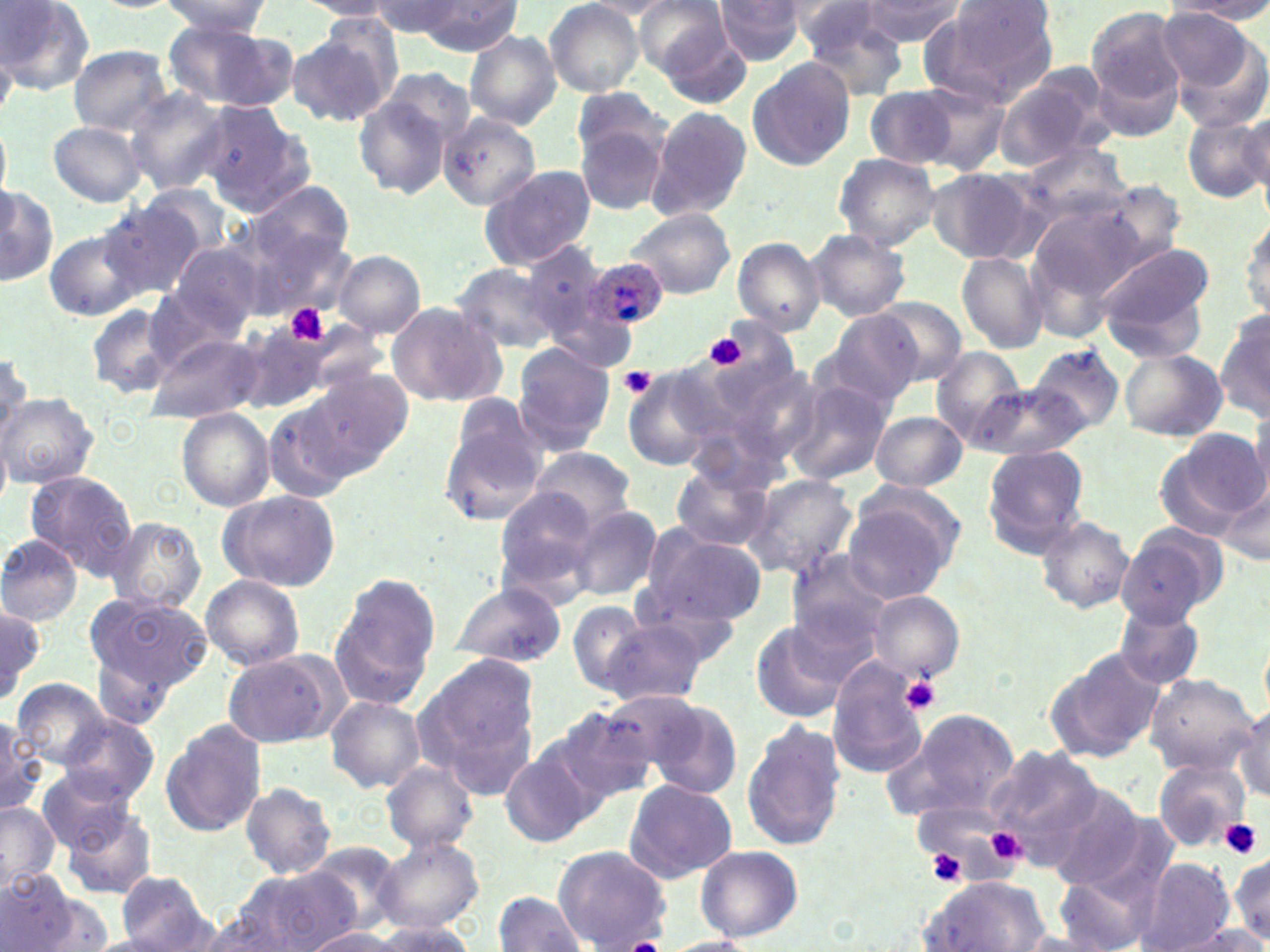
Approximate bounding boxes as named x1/y1/x2/y2 corners in pixels. Platelet locations: (x1=285, y1=303, x2=327, y2=345), (x1=695, y1=326, x2=761, y2=381), (x1=705, y1=336, x2=746, y2=369), (x1=620, y1=366, x2=657, y2=401), (x1=899, y1=676, x2=942, y2=714), (x1=1220, y1=818, x2=1263, y2=859), (x1=983, y1=825, x2=1026, y2=867), (x1=928, y1=849, x2=968, y2=885). Plasmodium ovale-infected red blood cell locations: (x1=583, y1=257, x2=670, y2=334). Uninfected red blood cell locations: (x1=0, y1=0, x2=95, y2=91), (x1=158, y1=0, x2=270, y2=39), (x1=371, y1=0, x2=463, y2=37), (x1=632, y1=0, x2=739, y2=83), (x1=859, y1=0, x2=963, y2=46), (x1=937, y1=0, x2=1060, y2=94), (x1=299, y1=1, x2=400, y2=20), (x1=544, y1=1, x2=645, y2=97), (x1=577, y1=1, x2=681, y2=17), (x1=713, y1=1, x2=806, y2=65), (x1=1166, y1=1, x2=1270, y2=20), (x1=414, y1=2, x2=522, y2=54), (x1=797, y1=3, x2=913, y2=98), (x1=158, y1=4, x2=280, y2=82), (x1=1160, y1=9, x2=1265, y2=108), (x1=1086, y1=10, x2=1187, y2=137), (x1=172, y1=24, x2=296, y2=111), (x1=286, y1=25, x2=397, y2=128), (x1=653, y1=27, x2=753, y2=108), (x1=465, y1=30, x2=562, y2=129), (x1=69, y1=46, x2=171, y2=135), (x1=746, y1=57, x2=857, y2=172), (x1=995, y1=70, x2=1109, y2=170), (x1=913, y1=83, x2=1012, y2=175), (x1=352, y1=87, x2=462, y2=200), (x1=571, y1=87, x2=669, y2=171), (x1=122, y1=88, x2=233, y2=196), (x1=865, y1=88, x2=961, y2=169), (x1=191, y1=102, x2=317, y2=215), (x1=643, y1=106, x2=753, y2=222), (x1=1241, y1=108, x2=1270, y2=195), (x1=440, y1=111, x2=541, y2=210), (x1=573, y1=114, x2=672, y2=219), (x1=1184, y1=115, x2=1269, y2=202), (x1=47, y1=121, x2=148, y2=207), (x1=1022, y1=141, x2=1132, y2=224), (x1=833, y1=153, x2=941, y2=248), (x1=478, y1=164, x2=597, y2=271), (x1=927, y1=166, x2=1047, y2=265), (x1=250, y1=181, x2=354, y2=268), (x1=1098, y1=181, x2=1189, y2=266), (x1=0, y1=183, x2=56, y2=289), (x1=139, y1=183, x2=235, y2=256), (x1=98, y1=202, x2=202, y2=299), (x1=1027, y1=204, x2=1148, y2=312), (x1=623, y1=207, x2=736, y2=298), (x1=1240, y1=212, x2=1270, y2=323), (x1=235, y1=220, x2=354, y2=321), (x1=46, y1=227, x2=147, y2=322), (x1=806, y1=228, x2=910, y2=321), (x1=733, y1=238, x2=826, y2=336), (x1=166, y1=240, x2=263, y2=336), (x1=521, y1=240, x2=613, y2=350), (x1=1098, y1=243, x2=1213, y2=355), (x1=333, y1=251, x2=425, y2=338), (x1=956, y1=252, x2=1048, y2=354), (x1=452, y1=262, x2=563, y2=357), (x1=867, y1=296, x2=968, y2=385), (x1=384, y1=299, x2=507, y2=407), (x1=86, y1=302, x2=182, y2=400), (x1=1216, y1=306, x2=1269, y2=424), (x1=817, y1=311, x2=924, y2=407), (x1=233, y1=327, x2=353, y2=413), (x1=147, y1=332, x2=262, y2=422), (x1=1025, y1=343, x2=1124, y2=438), (x1=512, y1=344, x2=615, y2=455), (x1=0, y1=347, x2=32, y2=446), (x1=1118, y1=347, x2=1227, y2=441), (x1=932, y1=348, x2=1025, y2=449), (x1=311, y1=368, x2=413, y2=468), (x1=623, y1=374, x2=720, y2=470), (x1=785, y1=379, x2=893, y2=485), (x1=974, y1=380, x2=1090, y2=463), (x1=2, y1=394, x2=99, y2=488), (x1=265, y1=401, x2=356, y2=500), (x1=179, y1=410, x2=276, y2=511), (x1=439, y1=410, x2=546, y2=525), (x1=870, y1=410, x2=969, y2=491), (x1=1156, y1=428, x2=1266, y2=539), (x1=982, y1=446, x2=1088, y2=555), (x1=526, y1=447, x2=638, y2=535), (x1=669, y1=463, x2=774, y2=551), (x1=25, y1=471, x2=138, y2=578), (x1=743, y1=474, x2=858, y2=580), (x1=1216, y1=478, x2=1269, y2=571), (x1=494, y1=486, x2=602, y2=595), (x1=218, y1=490, x2=340, y2=591), (x1=842, y1=500, x2=954, y2=603), (x1=568, y1=505, x2=662, y2=601), (x1=1035, y1=515, x2=1134, y2=613), (x1=105, y1=517, x2=207, y2=616), (x1=1116, y1=525, x2=1226, y2=628), (x1=641, y1=529, x2=767, y2=628), (x1=0, y1=535, x2=84, y2=627), (x1=785, y1=550, x2=895, y2=648), (x1=328, y1=571, x2=441, y2=709), (x1=202, y1=574, x2=304, y2=671), (x1=450, y1=584, x2=568, y2=667), (x1=631, y1=584, x2=743, y2=668), (x1=866, y1=591, x2=964, y2=681), (x1=86, y1=595, x2=213, y2=693), (x1=567, y1=599, x2=650, y2=693), (x1=783, y1=601, x2=886, y2=692), (x1=0, y1=603, x2=43, y2=703), (x1=1115, y1=605, x2=1205, y2=691), (x1=597, y1=619, x2=706, y2=707), (x1=749, y1=619, x2=855, y2=724), (x1=91, y1=647, x2=176, y2=730), (x1=1046, y1=647, x2=1166, y2=761), (x1=224, y1=650, x2=343, y2=750), (x1=413, y1=651, x2=541, y2=797), (x1=827, y1=665, x2=931, y2=778), (x1=1142, y1=673, x2=1257, y2=777), (x1=10, y1=676, x2=109, y2=767), (x1=618, y1=689, x2=743, y2=798), (x1=326, y1=695, x2=425, y2=793), (x1=1235, y1=701, x2=1270, y2=801), (x1=541, y1=705, x2=657, y2=812), (x1=881, y1=708, x2=1022, y2=826), (x1=56, y1=713, x2=159, y2=806), (x1=0, y1=717, x2=43, y2=816), (x1=740, y1=719, x2=848, y2=853), (x1=160, y1=720, x2=266, y2=838), (x1=498, y1=746, x2=598, y2=849), (x1=988, y1=747, x2=1105, y2=863), (x1=1152, y1=757, x2=1249, y2=852), (x1=381, y1=760, x2=477, y2=853), (x1=35, y1=769, x2=137, y2=856), (x1=623, y1=779, x2=737, y2=883), (x1=238, y1=783, x2=338, y2=879), (x1=1040, y1=784, x2=1152, y2=891), (x1=0, y1=801, x2=61, y2=891), (x1=61, y1=809, x2=157, y2=899), (x1=375, y1=833, x2=484, y2=933), (x1=306, y1=841, x2=407, y2=931), (x1=695, y1=845, x2=803, y2=941), (x1=552, y1=846, x2=671, y2=949), (x1=1229, y1=854, x2=1269, y2=943), (x1=1134, y1=859, x2=1236, y2=952), (x1=234, y1=867, x2=358, y2=951), (x1=1053, y1=868, x2=1158, y2=952), (x1=0, y1=869, x2=80, y2=951), (x1=112, y1=870, x2=217, y2=950), (x1=918, y1=876, x2=1053, y2=951), (x1=21, y1=888, x2=115, y2=952), (x1=490, y1=893, x2=587, y2=952), (x1=185, y1=911, x2=295, y2=952), (x1=368, y1=920, x2=479, y2=951), (x1=1163, y1=925, x2=1270, y2=952), (x1=302, y1=929, x2=408, y2=951), (x1=660, y1=936, x2=763, y2=952). Slide-level diagnosis: Plasmodium ovale. Optical microscopy. Thin blood film. Captured at 1000x magnification. One field of a larger specimen. Image is 1270×952 pixels. May-Grünwald-Giemsa stain.